Locate every Plasmodium ovale-infected red blood cell.
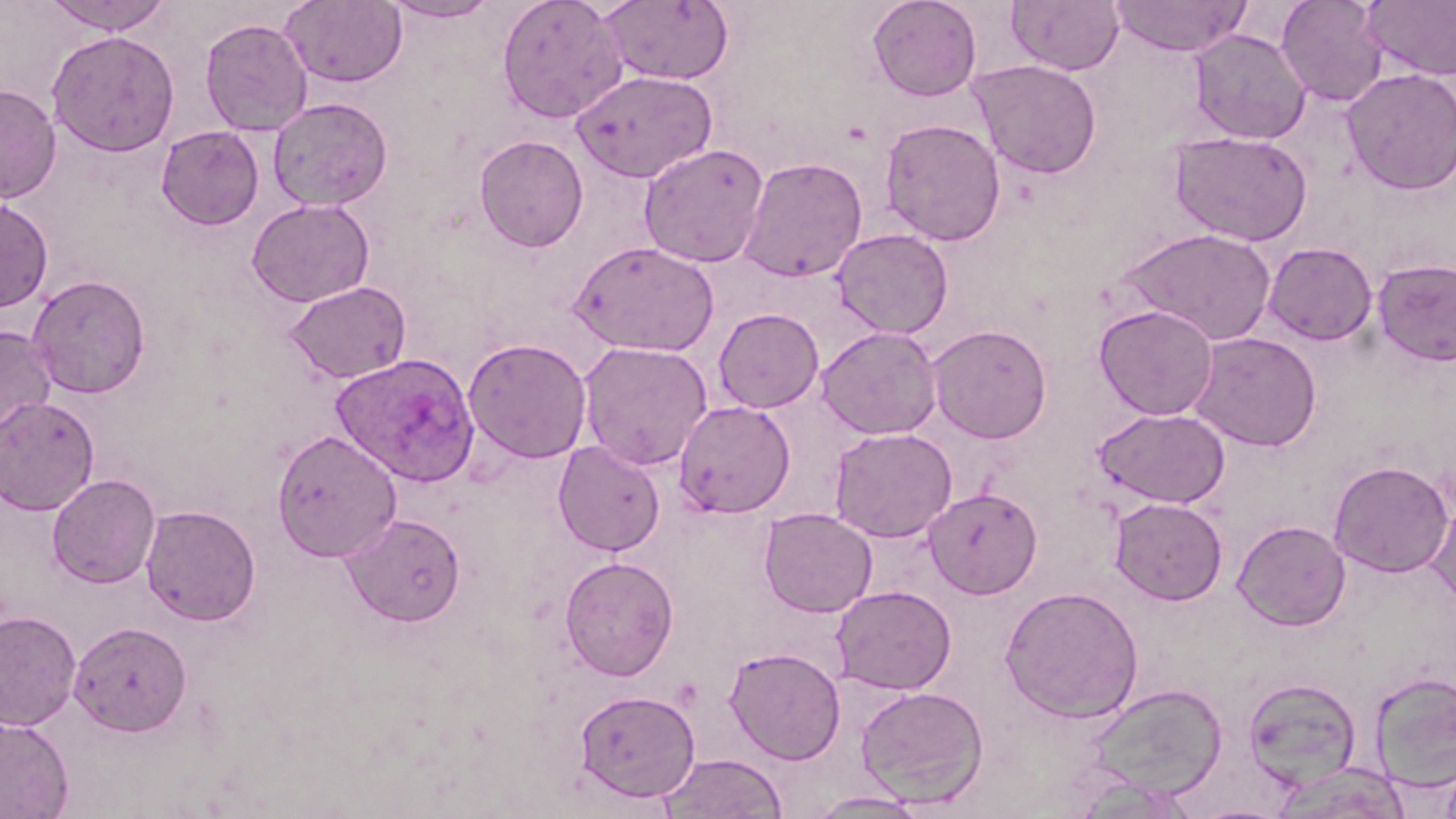
Approximate bounding boxes as [x1, y1, x2, y2] in pixels.
Plasmodium ovale-infected red blood cells: [331, 353, 480, 487].

Summary:
  - Uninfected red blood cell locations: [43, 0, 174, 34], [281, 0, 408, 88], [383, 0, 500, 23], [496, 0, 629, 124], [600, 0, 735, 86], [867, 0, 982, 101], [1006, 0, 1126, 75], [1110, 0, 1252, 57], [1276, 0, 1389, 106], [1363, 0, 1456, 80], [199, 18, 314, 136], [1188, 28, 1311, 144], [46, 30, 180, 157], [969, 59, 1102, 178], [1342, 68, 1456, 194], [571, 70, 717, 183], [0, 84, 61, 203], [268, 98, 393, 210], [879, 117, 1006, 246], [156, 126, 264, 229], [1169, 131, 1313, 246], [474, 135, 588, 253], [639, 143, 770, 268], [738, 156, 868, 283], [0, 197, 53, 312], [247, 198, 374, 307], [1117, 227, 1278, 344], [832, 228, 953, 339], [569, 239, 720, 356], [1264, 242, 1378, 346], [1372, 258, 1456, 366], [28, 275, 150, 398], [284, 281, 411, 384], [1094, 304, 1219, 420], [713, 308, 824, 413], [0, 324, 57, 449], [928, 324, 1052, 443], [816, 326, 943, 439], [1191, 332, 1322, 451], [463, 337, 592, 464], [577, 341, 713, 471], [0, 395, 100, 515], [673, 400, 796, 518], [1095, 407, 1230, 509], [829, 427, 957, 542], [272, 429, 402, 563], [553, 440, 666, 556], [1329, 460, 1454, 577], [47, 474, 160, 588], [923, 487, 1043, 599], [1109, 497, 1228, 605], [1427, 499, 1456, 610], [140, 505, 261, 626], [758, 508, 878, 618], [343, 512, 466, 626], [1232, 519, 1351, 631], [559, 555, 679, 681], [831, 584, 957, 695], [1000, 585, 1144, 723], [0, 609, 81, 731], [69, 621, 192, 736], [725, 646, 846, 765], [1369, 671, 1456, 792], [1243, 677, 1362, 791], [1083, 683, 1229, 801], [856, 685, 989, 808], [574, 688, 700, 802], [0, 716, 74, 819], [659, 753, 787, 818], [1270, 761, 1411, 819], [806, 790, 932, 817]
  - Slide-level diagnosis: Plasmodium ovale
  - Preparation: thin blood smear
  - Image size: 1456×819 pixels
  - Magnification: 1000x
  - Modality: light microscopy
  - Field of view: single
  - Stain: May-Grünwald-Giemsa